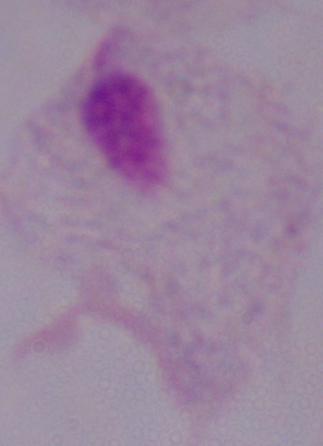
identification = trichomonad
modality = micrograph
magnification = 1000x